Assess the morphology of the red blood cells.
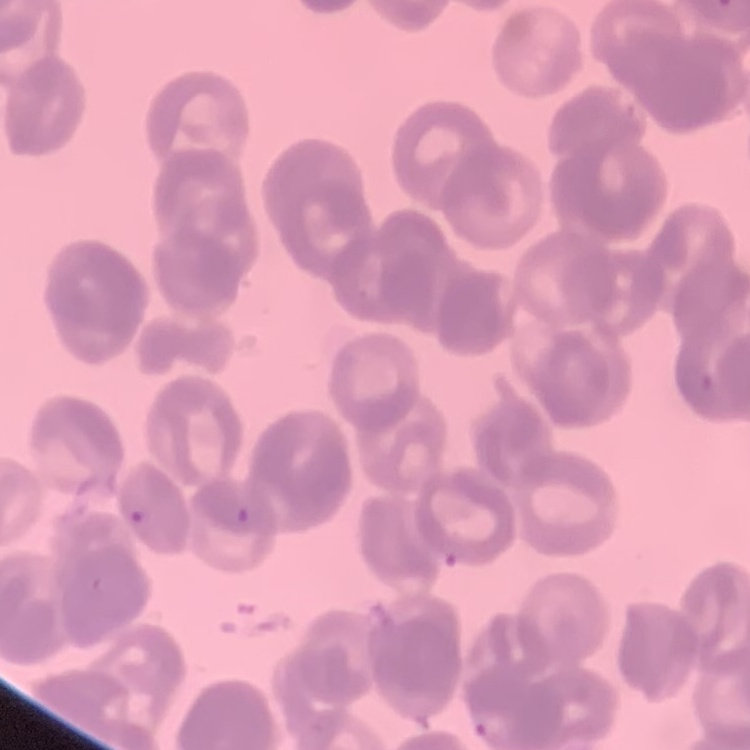

They show rouleaux formation.

preparation: thin blood film
stain: Field's or Giemsa
image_type: one tile cut from a larger photomicrograph